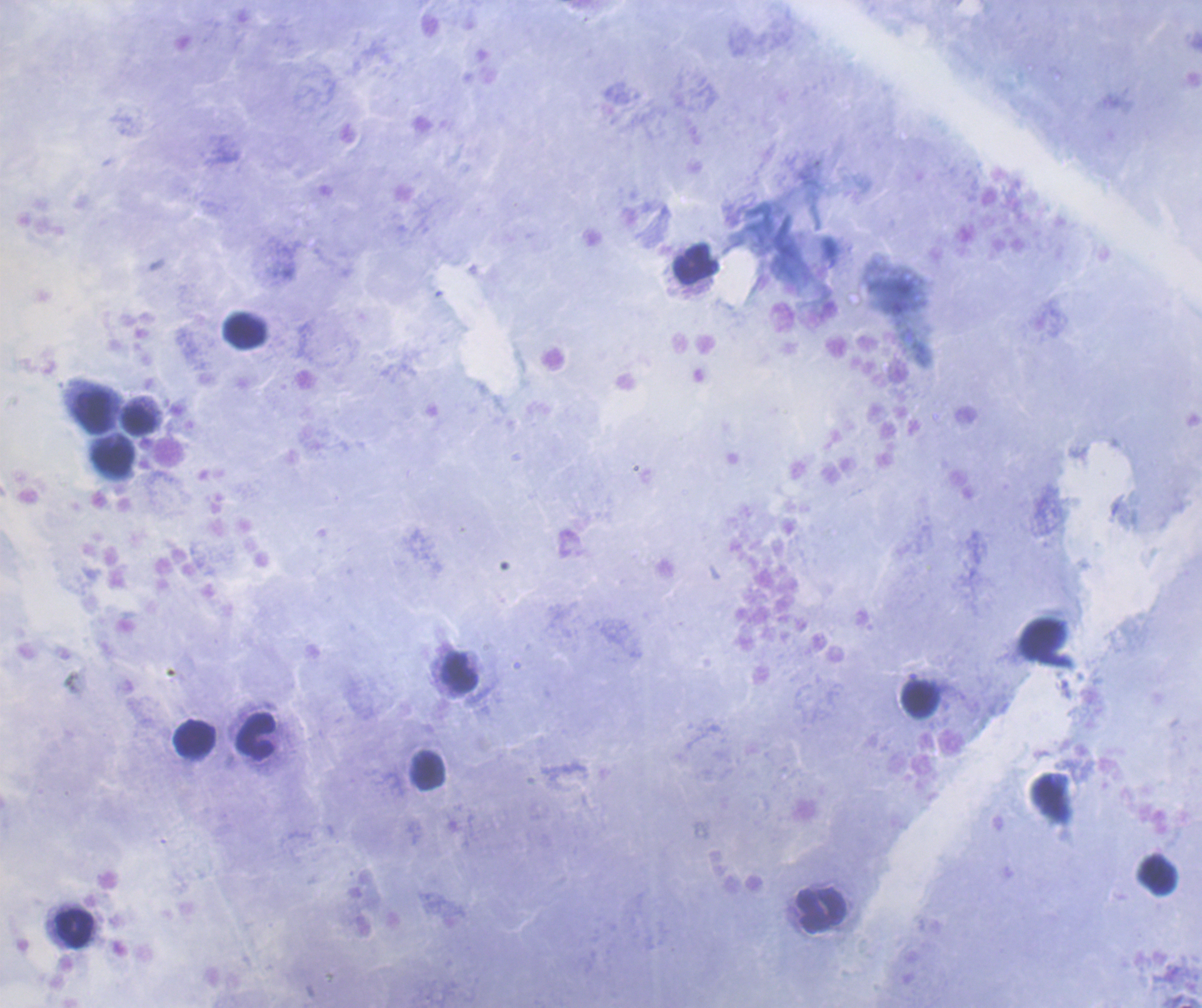 Approximate centers as (x, y) in pixels. Leukocyte locations: (696, 264), (244, 329), (94, 413), (140, 420), (113, 460), (460, 673), (920, 699), (256, 737), (195, 738), (428, 771), (1158, 876), (822, 911), (74, 928). Result: negative for Plasmodium parasites. Romanowsky-stained preparation. Background quality: satisfactory. Single field of view. Coloration quality: good. 100x magnification. Previously used in an actual diagnosis. Thick blood smear. Image is 1202×1008 pixels.